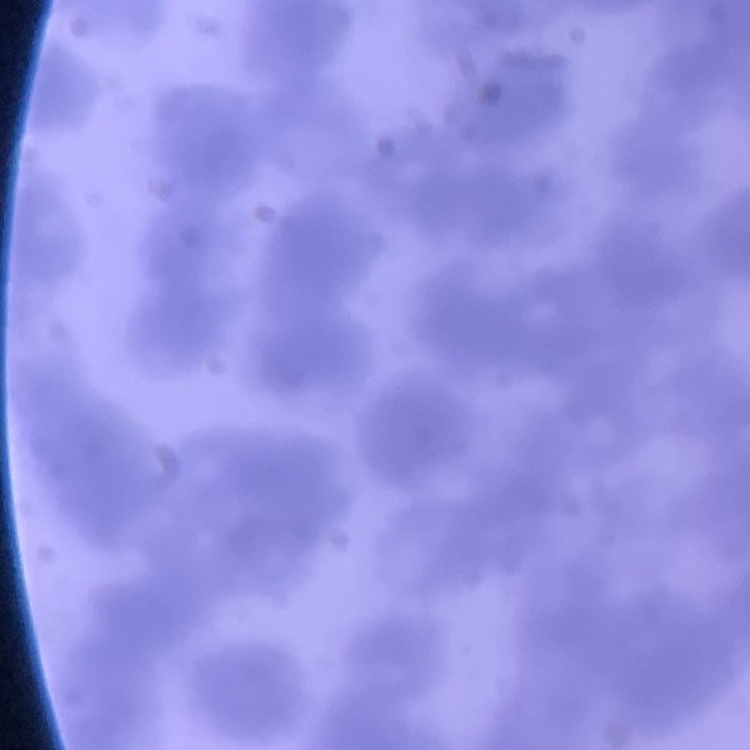
erythrocyte_morphology: rouleaux formation
image_type: square crop of a larger photomicrograph
stain: Field's or Giemsa
preparation: thin blood film